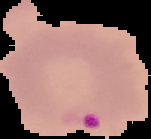 From a thin blood film. Segmented cell region on a black background. Malaria status: parasitized. Image is 151×139 pixels.